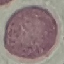

Result: no malaria parasites seen. Automatically extracted cell patch, resized to 64 × 64 pixels. Acquired by smartphone through the microscope eyepiece. Giemsa stain. Thin smear of blood.